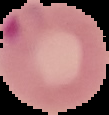

{
  "result": "Plasmodium parasites identified",
  "image_size": "109×115 pixels",
  "image_type": "segmented cell region with the area outside set to black",
  "preparation": "thin blood smear"
}